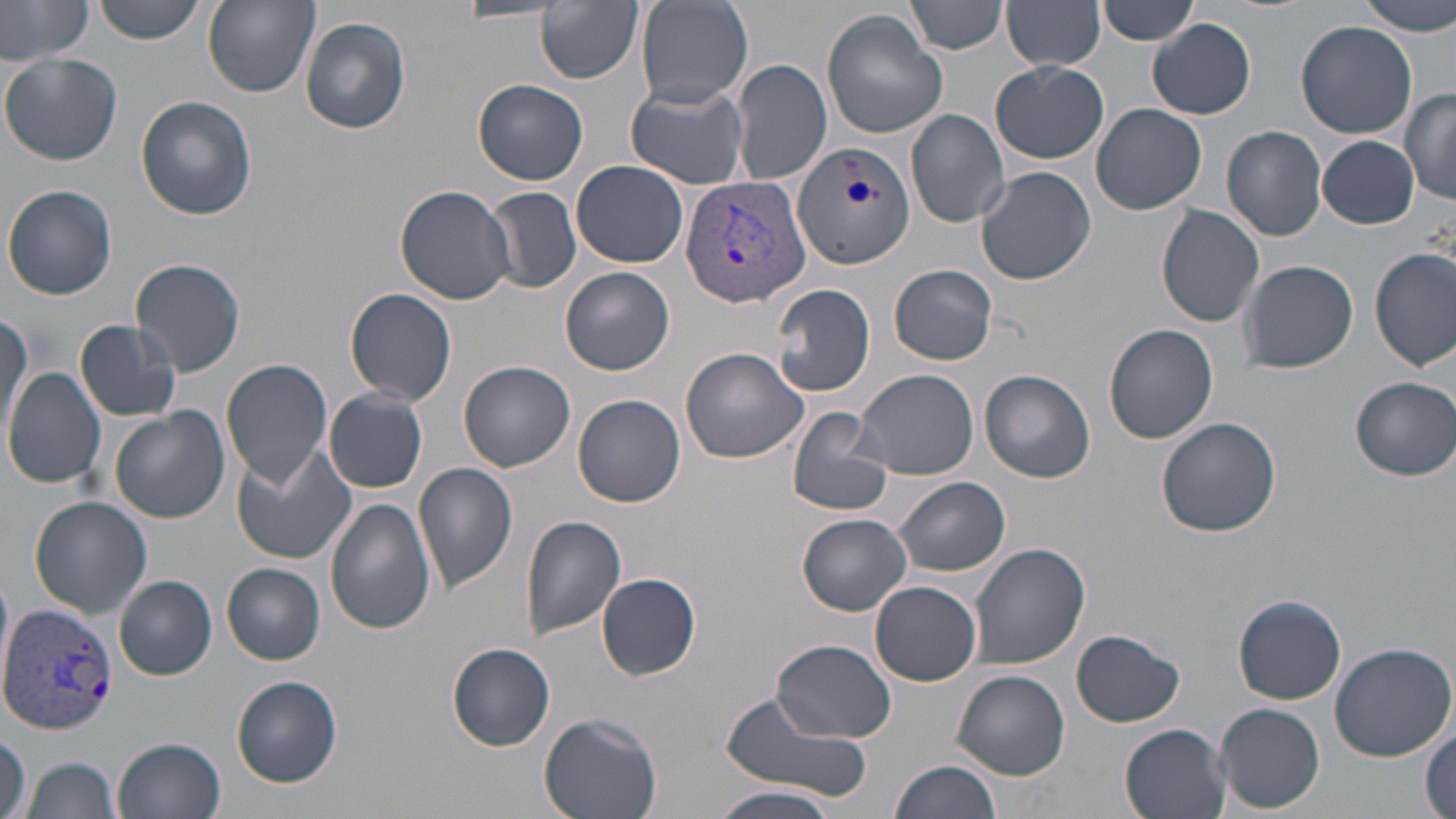

Summary:
  - Coordinate format: approximate bounding boxes as (x1,y1)-(x2,y2) corner pairs in pixels
  - Uninfected red blood cell locations: (0,0)-(94,64), (90,0)-(208,44), (202,0)-(318,98), (905,0)-(1007,55), (1095,0)-(1202,45), (1359,0)-(1455,33), (535,1)-(642,84), (634,1)-(753,109), (1003,3)-(1106,71), (820,9)-(950,139), (301,16)-(412,134), (1148,19)-(1256,120), (1296,20)-(1418,137), (1,54)-(122,166), (731,59)-(832,186), (990,61)-(1108,164), (475,77)-(588,185), (626,83)-(750,189), (1403,89)-(1456,206), (138,97)-(255,221), (1092,104)-(1208,215), (906,108)-(1010,230), (1221,126)-(1329,242), (1317,135)-(1419,229), (572,159)-(690,267), (976,167)-(1096,285), (4,185)-(117,300), (395,185)-(516,305), (485,187)-(581,294), (1156,206)-(1265,329), (1370,248)-(1454,370), (1240,259)-(1359,373), (131,260)-(247,376), (890,264)-(997,364), (562,267)-(675,376), (772,283)-(878,397), (345,288)-(458,407), (0,312)-(32,442), (75,320)-(183,422), (1104,323)-(1218,444), (681,347)-(808,462), (221,358)-(333,487), (459,362)-(575,471), (3,367)-(106,489), (853,368)-(979,479), (980,369)-(1095,482), (1350,378)-(1455,480), (324,391)-(429,492), (573,394)-(685,507), (110,406)-(231,525), (785,406)-(896,517), (1157,418)-(1282,538), (231,447)-(358,564), (413,462)-(518,592), (895,477)-(1010,576), (30,497)-(152,619), (325,497)-(434,635), (519,513)-(626,641), (798,513)-(912,615), (967,542)-(1090,669), (222,563)-(326,664), (0,567)-(15,696), (598,574)-(700,681), (115,576)-(217,681), (870,580)-(983,686), (1234,595)-(1346,704), (1071,630)-(1185,727), (773,640)-(895,743), (1328,641)-(1456,761), (447,643)-(556,751), (952,670)-(1069,780), (231,675)-(341,786), (720,690)-(875,803), (1214,703)-(1325,814), (539,712)-(663,819), (1120,722)-(1232,819), (1421,727)-(1455,819), (0,731)-(30,819), (115,736)-(226,819), (25,758)-(121,819), (890,758)-(1004,819), (711,786)-(843,819)
  - Plasmodium vivax-infected red blood cell locations: (792,141)-(914,267), (681,175)-(810,308), (1,605)-(116,735)
  - Slide-level diagnosis: Plasmodium vivax
  - Magnification: 1000x
  - Preparation: thin blood smear
  - Stain: May-Grünwald-Giemsa
  - Image size: 1456×819 pixels
  - Modality: optical microscopy
  - Field of view: single